Identify the blood parasite species.
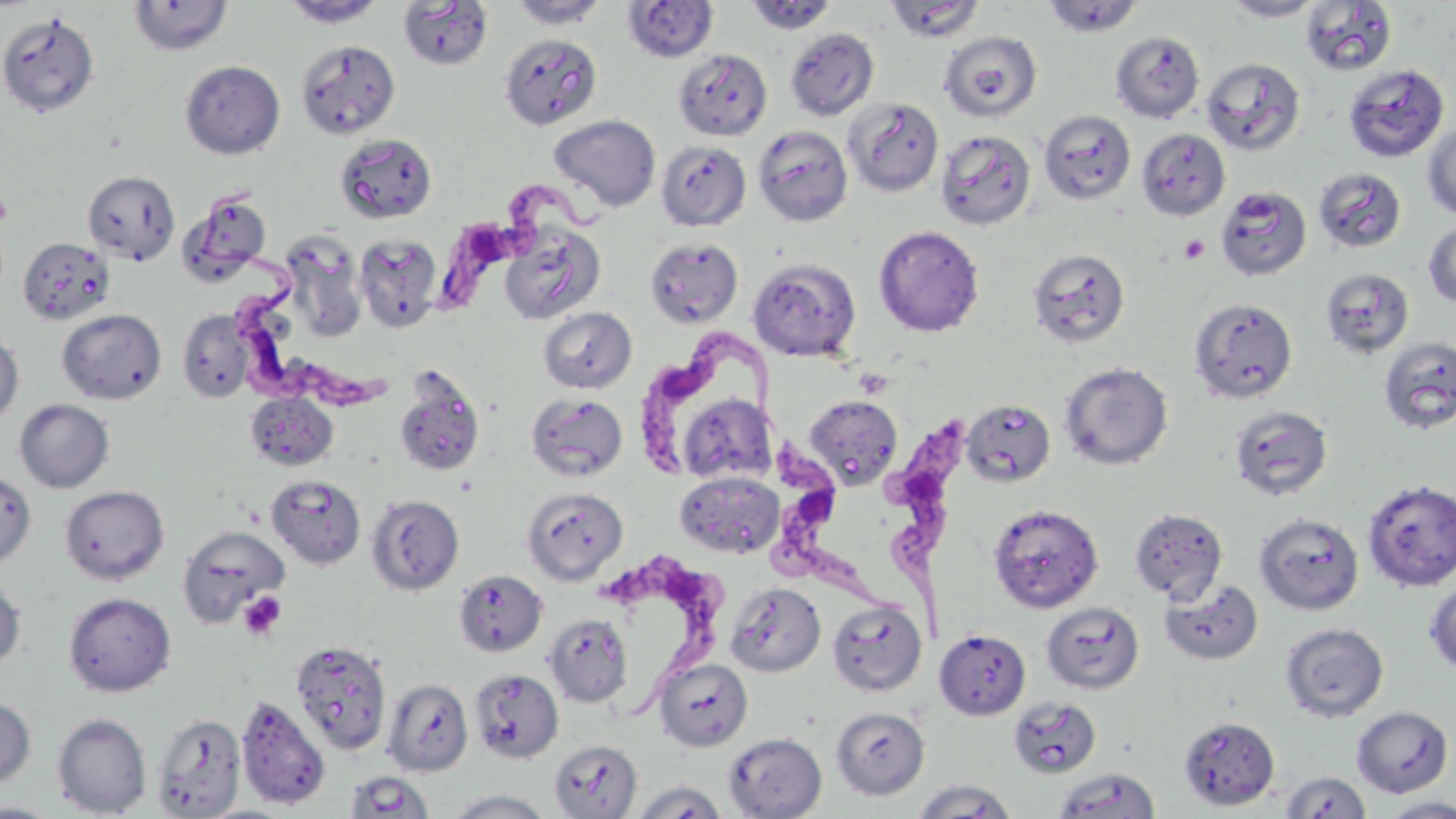

Trypanosoma brucei.

preparation = thin blood film
stain = May-Grünwald-Giemsa
platelet locations = approximate bounding boxes as named x1/y1/x2/y2 corners in pixels: (x1=0, y1=190, x2=13, y2=226), (x1=1179, y1=234, x2=1210, y2=264), (x1=238, y1=591, x2=286, y2=641)
field of view = single
Trypanosoma brucei locations = approximate bounding boxes as named x1/y1/x2/y2 corners in pixels: (x1=445, y1=179, x2=605, y2=304), (x1=196, y1=190, x2=397, y2=408), (x1=638, y1=321, x2=798, y2=483), (x1=887, y1=417, x2=972, y2=641), (x1=776, y1=440, x2=885, y2=633), (x1=605, y1=553, x2=728, y2=715)
magnification = 1000x
uninfected red blood cell locations = approximate bounding boxes as named x1/y1/x2/y2 corners in pixels: (x1=127, y1=0, x2=234, y2=56), (x1=280, y1=0, x2=387, y2=28), (x1=507, y1=0, x2=610, y2=29), (x1=1041, y1=0, x2=1145, y2=38), (x1=1221, y1=0, x2=1326, y2=21), (x1=397, y1=1, x2=494, y2=71), (x1=621, y1=1, x2=719, y2=62), (x1=743, y1=1, x2=839, y2=35), (x1=883, y1=1, x2=985, y2=42), (x1=1300, y1=1, x2=1397, y2=76), (x1=0, y1=11, x2=100, y2=118), (x1=784, y1=27, x2=880, y2=121), (x1=939, y1=30, x2=1042, y2=123), (x1=1110, y1=31, x2=1204, y2=123), (x1=499, y1=33, x2=603, y2=130), (x1=295, y1=40, x2=401, y2=140), (x1=672, y1=49, x2=773, y2=141), (x1=1201, y1=57, x2=1306, y2=156), (x1=179, y1=60, x2=285, y2=159), (x1=1342, y1=63, x2=1450, y2=162), (x1=843, y1=98, x2=944, y2=197), (x1=1038, y1=109, x2=1136, y2=205), (x1=548, y1=114, x2=661, y2=212), (x1=1422, y1=121, x2=1456, y2=221), (x1=752, y1=125, x2=853, y2=227), (x1=1136, y1=128, x2=1231, y2=220), (x1=935, y1=129, x2=1036, y2=231), (x1=335, y1=133, x2=438, y2=223), (x1=656, y1=141, x2=751, y2=231), (x1=1312, y1=167, x2=1407, y2=254), (x1=82, y1=170, x2=180, y2=265), (x1=1215, y1=184, x2=1312, y2=281), (x1=1423, y1=219, x2=1456, y2=309), (x1=498, y1=223, x2=606, y2=325), (x1=873, y1=225, x2=985, y2=337), (x1=353, y1=234, x2=443, y2=332), (x1=17, y1=236, x2=115, y2=326), (x1=644, y1=237, x2=743, y2=329), (x1=1026, y1=247, x2=1130, y2=347), (x1=748, y1=258, x2=861, y2=362), (x1=1319, y1=268, x2=1414, y2=357), (x1=1187, y1=298, x2=1298, y2=404), (x1=538, y1=306, x2=637, y2=393), (x1=57, y1=308, x2=167, y2=405), (x1=177, y1=309, x2=254, y2=402), (x1=0, y1=332, x2=24, y2=428), (x1=1378, y1=336, x2=1456, y2=434), (x1=1058, y1=361, x2=1173, y2=471), (x1=394, y1=368, x2=486, y2=477), (x1=245, y1=391, x2=338, y2=471), (x1=526, y1=393, x2=628, y2=482), (x1=803, y1=395, x2=903, y2=489), (x1=14, y1=399, x2=115, y2=493), (x1=962, y1=399, x2=1055, y2=487), (x1=682, y1=400, x2=784, y2=486), (x1=1228, y1=405, x2=1333, y2=500), (x1=0, y1=470, x2=37, y2=571), (x1=675, y1=471, x2=785, y2=558), (x1=266, y1=474, x2=366, y2=569), (x1=1362, y1=479, x2=1456, y2=591), (x1=59, y1=485, x2=169, y2=585), (x1=521, y1=487, x2=628, y2=585), (x1=366, y1=494, x2=464, y2=596), (x1=988, y1=503, x2=1103, y2=613), (x1=1129, y1=507, x2=1228, y2=603), (x1=1254, y1=512, x2=1364, y2=615), (x1=176, y1=524, x2=290, y2=628), (x1=454, y1=569, x2=548, y2=657), (x1=1160, y1=576, x2=1264, y2=666), (x1=0, y1=577, x2=26, y2=671), (x1=1425, y1=579, x2=1456, y2=675), (x1=725, y1=582, x2=826, y2=677), (x1=63, y1=592, x2=176, y2=696), (x1=827, y1=600, x2=926, y2=696), (x1=1041, y1=601, x2=1144, y2=694), (x1=544, y1=613, x2=634, y2=707), (x1=1280, y1=622, x2=1389, y2=722), (x1=934, y1=629, x2=1031, y2=720), (x1=289, y1=639, x2=392, y2=756), (x1=654, y1=658, x2=753, y2=751), (x1=470, y1=669, x2=564, y2=764), (x1=381, y1=678, x2=473, y2=776), (x1=235, y1=696, x2=331, y2=811), (x1=0, y1=697, x2=36, y2=789), (x1=1008, y1=697, x2=1101, y2=778), (x1=1351, y1=706, x2=1453, y2=797), (x1=830, y1=707, x2=930, y2=800), (x1=150, y1=712, x2=246, y2=818), (x1=52, y1=713, x2=151, y2=816), (x1=1178, y1=716, x2=1280, y2=811), (x1=723, y1=732, x2=827, y2=819), (x1=549, y1=739, x2=642, y2=818), (x1=1053, y1=768, x2=1161, y2=819), (x1=345, y1=770, x2=435, y2=818), (x1=1280, y1=771, x2=1371, y2=818), (x1=912, y1=779, x2=1017, y2=818), (x1=629, y1=780, x2=728, y2=819), (x1=444, y1=788, x2=557, y2=818), (x1=1381, y1=797, x2=1456, y2=818), (x1=0, y1=801, x2=65, y2=818)
image size = 1456×819 pixels
modality = light microscopy